Assess the morphology of the red blood cells.
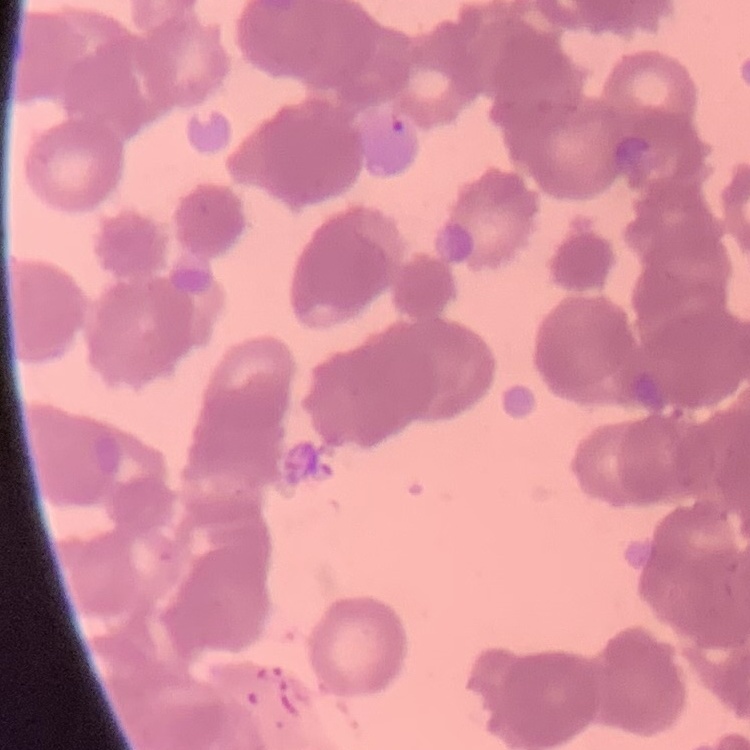
They show rouleaux formation.

Summary:
  - Preparation: thin peripheral smear
  - Image type: square crop of a larger photomicrograph
  - Stain: Field's or Giemsa